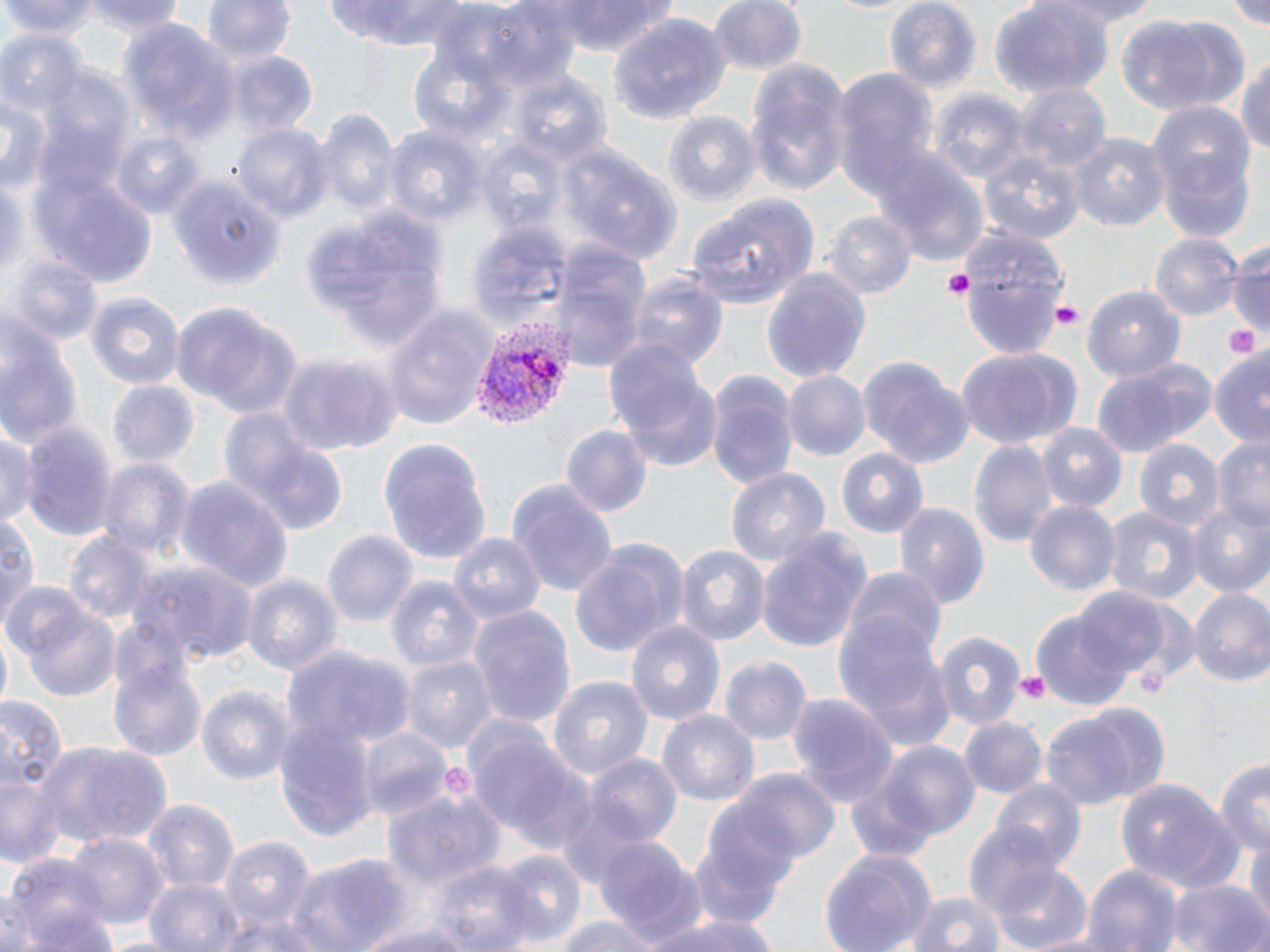
Summary:
  - Coordinate format: approximate bounding boxes as [x1, y1, x2, y2] in pixels
  - Uninfected red blood cell locations: [3, 0, 105, 40], [85, 0, 188, 37], [199, 0, 293, 69], [321, 0, 478, 49], [541, 0, 679, 55], [706, 0, 806, 79], [991, 0, 1115, 98], [1035, 0, 1157, 34], [1226, 0, 1270, 31], [882, 1, 982, 94], [1115, 11, 1245, 116], [609, 15, 733, 127], [121, 22, 240, 147], [3, 32, 81, 114], [1235, 50, 1270, 164], [229, 53, 320, 136], [744, 59, 852, 195], [833, 69, 941, 203], [41, 71, 135, 173], [513, 75, 612, 169], [1014, 83, 1108, 174], [930, 90, 1027, 190], [1, 96, 51, 193], [1148, 104, 1256, 237], [317, 109, 399, 224], [663, 111, 758, 206], [232, 123, 331, 226], [385, 124, 487, 228], [108, 127, 208, 221], [1067, 133, 1169, 235], [560, 140, 683, 265], [981, 152, 1087, 246], [874, 159, 991, 268], [0, 171, 27, 288], [169, 175, 283, 291], [36, 178, 154, 285], [687, 194, 819, 309], [297, 202, 450, 353], [822, 210, 916, 299], [466, 221, 571, 334], [953, 229, 1070, 360], [1151, 232, 1242, 320], [553, 243, 648, 370], [1229, 243, 1270, 345], [7, 255, 103, 350], [761, 267, 872, 383], [627, 274, 727, 373], [1082, 282, 1186, 383], [85, 291, 183, 392], [171, 302, 303, 419], [382, 306, 497, 429], [0, 328, 87, 453], [603, 338, 719, 473], [954, 348, 1082, 451], [1207, 348, 1270, 453], [855, 353, 972, 469], [276, 354, 398, 457], [1091, 358, 1215, 457], [705, 370, 799, 490], [784, 370, 870, 461], [105, 380, 201, 471], [578, 381, 687, 510], [216, 405, 345, 534], [20, 421, 119, 545], [0, 422, 38, 533], [1037, 423, 1126, 513], [560, 424, 652, 519], [378, 438, 491, 563], [1214, 438, 1270, 535], [969, 439, 1057, 547], [1134, 440, 1225, 536], [833, 446, 928, 538], [99, 456, 193, 560], [724, 464, 832, 571], [175, 475, 293, 591], [507, 479, 619, 598], [1025, 501, 1120, 600], [894, 502, 988, 609], [1187, 503, 1270, 601], [1104, 505, 1202, 605], [2, 511, 39, 630], [323, 530, 419, 633], [757, 531, 873, 653], [66, 532, 159, 628], [449, 533, 545, 628], [571, 541, 685, 656], [674, 544, 767, 648], [136, 562, 259, 667], [846, 569, 949, 668], [242, 573, 342, 680], [388, 575, 486, 673], [1072, 587, 1172, 679], [1187, 590, 1270, 688], [836, 591, 956, 752], [17, 593, 122, 703], [468, 605, 576, 730], [1031, 610, 1134, 712], [625, 619, 726, 730], [932, 630, 1025, 732], [288, 643, 411, 752], [109, 654, 210, 763], [719, 654, 811, 745], [405, 656, 497, 755], [546, 675, 653, 785], [197, 685, 295, 788], [786, 692, 900, 810], [0, 697, 66, 795], [1042, 701, 1169, 808], [657, 708, 758, 810], [960, 715, 1046, 796], [277, 716, 376, 839], [466, 723, 592, 853], [357, 727, 453, 822], [34, 739, 174, 848], [868, 739, 981, 842], [584, 753, 684, 851], [0, 755, 68, 871], [1214, 758, 1270, 856], [730, 769, 839, 866], [992, 777, 1086, 871], [1115, 777, 1242, 899], [384, 786, 505, 891], [142, 797, 240, 896], [686, 819, 794, 937], [963, 821, 1062, 919], [1241, 827, 1270, 928], [66, 833, 165, 930], [591, 836, 709, 946], [220, 837, 313, 931], [819, 847, 937, 952], [490, 850, 588, 947], [5, 853, 112, 952], [286, 853, 406, 952], [423, 862, 535, 950], [1081, 864, 1183, 952], [994, 865, 1096, 952], [144, 877, 245, 952], [1169, 877, 1266, 952], [900, 889, 1009, 952], [217, 911, 326, 952], [644, 911, 779, 952], [550, 913, 673, 952], [355, 917, 485, 951]
  - Platelet locations: [941, 272, 972, 301], [1051, 302, 1081, 330], [1225, 321, 1261, 360], [1015, 671, 1050, 703]
  - Plasmodium vivax-infected red blood cell locations: [467, 321, 572, 429]
  - Slide-level diagnosis: Plasmodium vivax
  - Field of view: one of a larger specimen
  - Stain: May-Grünwald-Giemsa
  - Modality: light microscopy
  - Preparation: thin blood film
  - Image size: 1270×952 pixels
  - Magnification: 1000x